Name the parasite shown.
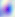
Toxoplasma gondii.

magnification: 400x
modality: micrograph